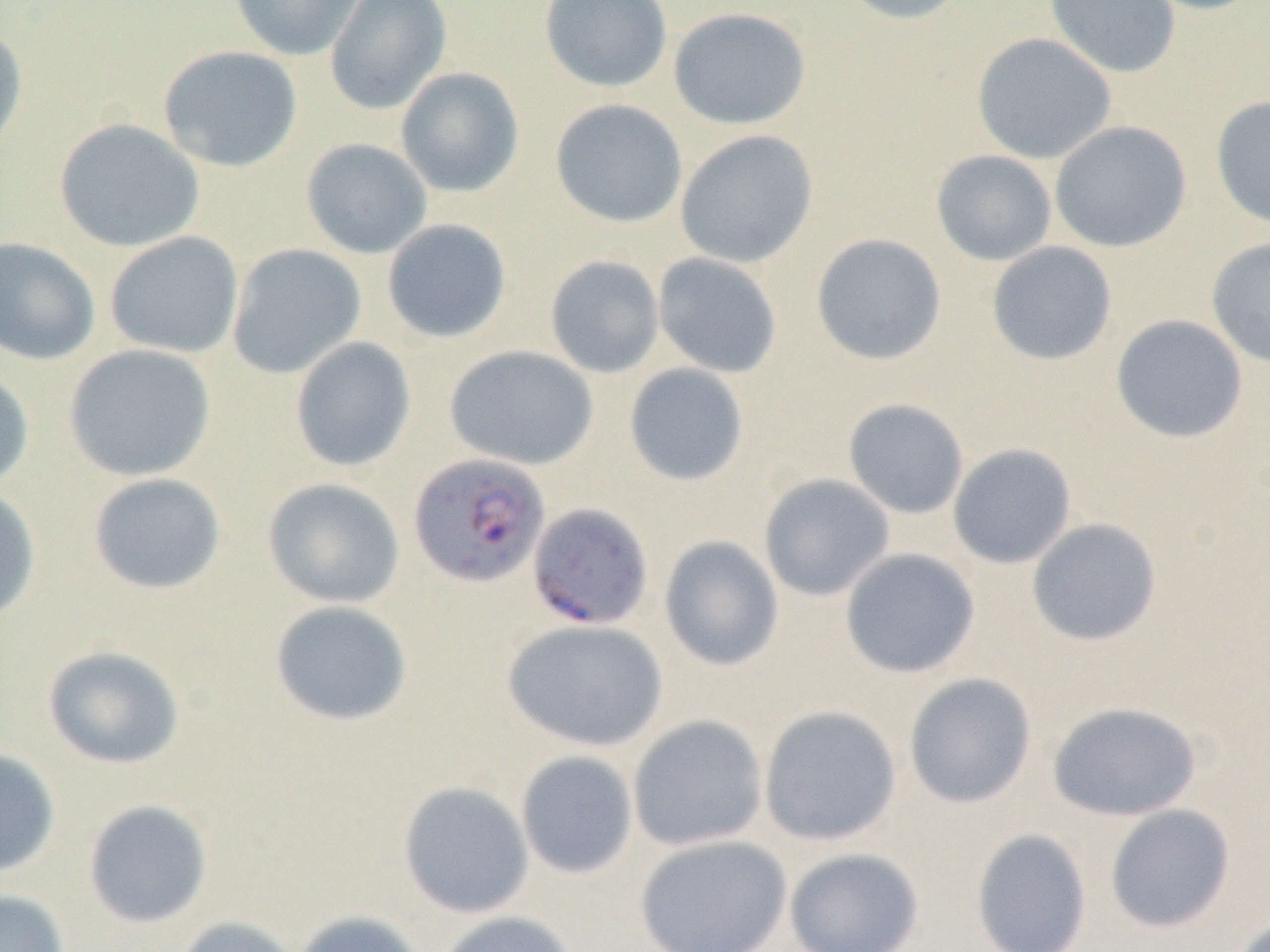

Approximate bounding boxes as (x1,y1)-(x2,y2) corner pairs in pixels. Uninfected red blood cell locations: (229,0)-(367,61), (324,0)-(452,115), (539,0)-(673,93), (836,0)-(971,25), (1045,0)-(1181,79), (1134,0)-(1268,16), (667,6)-(812,130), (0,25)-(29,162), (971,32)-(1117,164), (158,45)-(303,173), (395,67)-(525,198), (1210,95)-(1270,229), (550,98)-(688,228), (53,118)-(205,253), (1049,120)-(1192,253), (675,129)-(819,268), (300,138)-(433,259), (931,150)-(1058,266), (382,219)-(512,344), (104,231)-(244,359), (810,233)-(947,366), (0,237)-(101,365), (1205,237)-(1270,369), (986,241)-(1118,366), (226,243)-(367,380), (652,252)-(783,379), (544,255)-(665,378), (1110,314)-(1248,444), (289,336)-(417,473), (63,344)-(216,482), (443,345)-(599,471), (623,363)-(750,486), (0,368)-(34,492), (842,398)-(970,519), (947,443)-(1077,569), (87,472)-(227,595), (758,473)-(895,601), (262,478)-(405,609), (0,485)-(41,623), (1026,517)-(1162,647), (659,536)-(784,671), (839,548)-(981,678), (269,600)-(413,727), (501,618)-(669,752), (42,645)-(186,770), (902,673)-(1037,809), (1046,700)-(1203,821), (758,705)-(902,846), (628,715)-(769,851), (0,747)-(61,877), (515,750)-(638,879), (397,781)-(534,918), (83,799)-(212,929), (1104,804)-(1236,934), (970,828)-(1092,952), (633,834)-(793,951), (783,847)-(925,952), (0,889)-(71,952), (291,909)-(426,952), (434,910)-(578,952), (1226,912)-(1269,952), (174,915)-(302,952). Plasmodium falciparum-infected red blood cell locations: (408,452)-(551,588), (527,502)-(654,631). Slide-level diagnosis: Plasmodium falciparum. 1000x magnification. Thin blood film. Image is 1270×952 pixels. Single field of view. Optical microscopy.